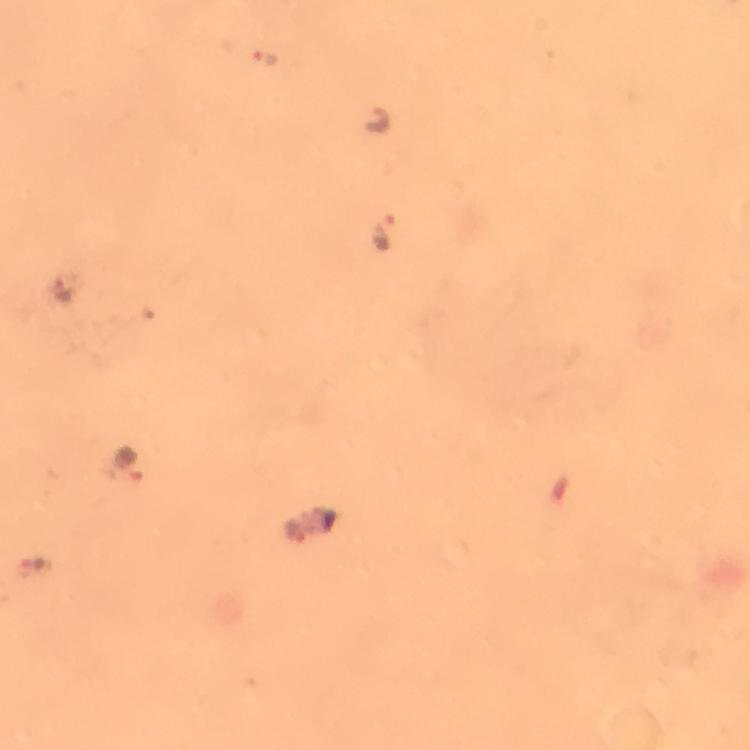

Approximate centers as (x, y) in pixels. Plasmodium parasite locations: (266, 61), (385, 226), (131, 467), (293, 531). From a malaria diagnostic workup. Immersion oil was used. Thick blood film. At 100x magnification. Image is 750×750 pixels. Giemsa-stained preparation. Photographed through the microscope with a smartphone camera. Cropped region of a single field of view.